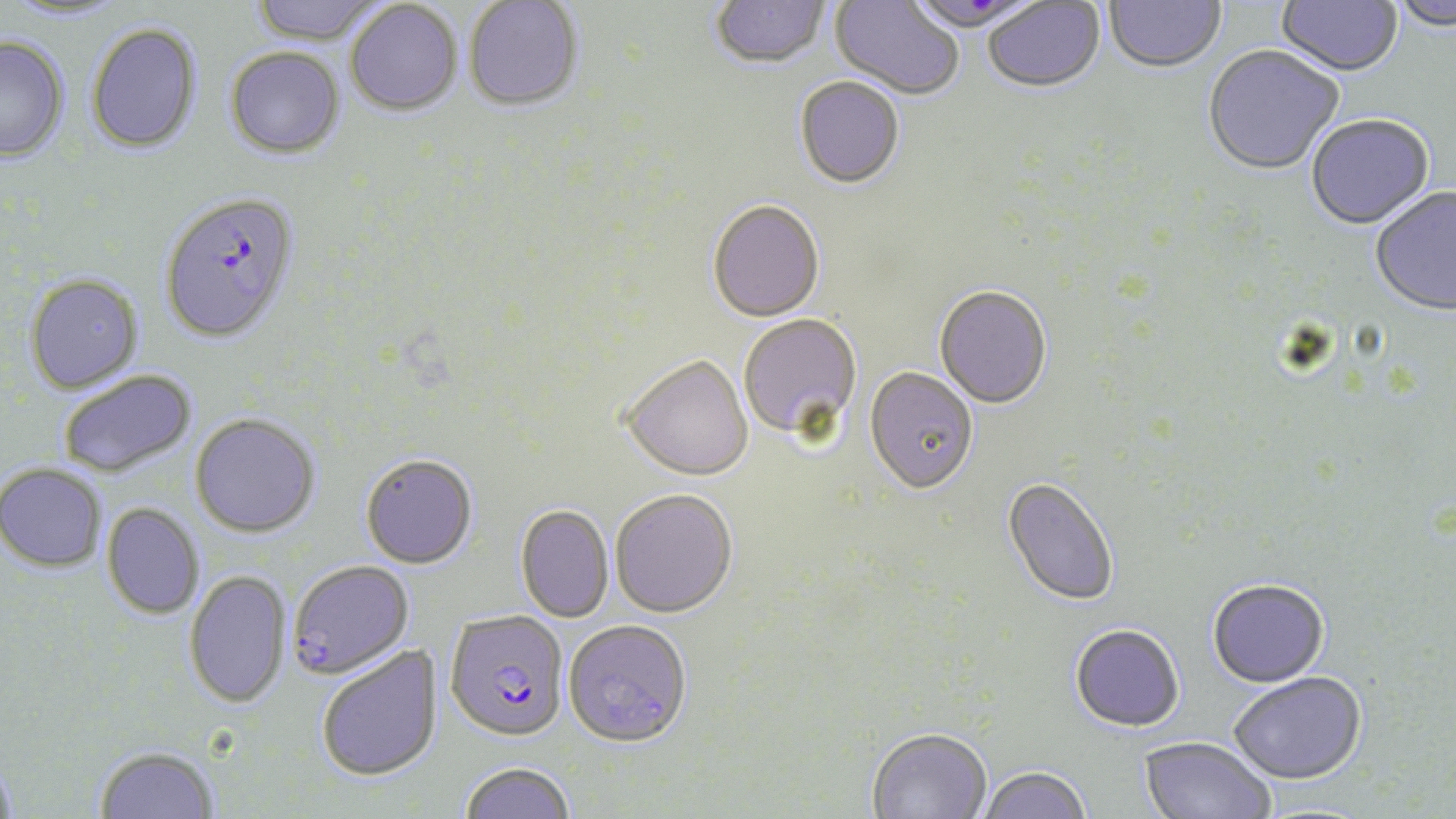 Approximate bounding boxes as [x1, y1, x2, y2] in pixels. Plasmodium falciparum-infected red blood cell locations: [159, 192, 300, 343], [288, 560, 414, 679], [444, 611, 569, 744]. Uninfected red blood cell locations: [3, 0, 130, 23], [249, 0, 389, 46], [1104, 0, 1226, 76], [1276, 0, 1404, 79], [464, 1, 584, 114], [711, 1, 830, 72], [829, 1, 964, 102], [983, 1, 1106, 96], [1390, 1, 1456, 34], [345, 2, 463, 118], [85, 22, 202, 153], [0, 36, 69, 161], [224, 47, 346, 160], [1203, 47, 1344, 177], [794, 78, 904, 191], [1306, 117, 1434, 232], [1370, 188, 1456, 319], [707, 202, 825, 324], [24, 273, 143, 393], [934, 288, 1052, 411], [738, 315, 863, 445], [621, 357, 753, 483], [864, 369, 978, 497], [58, 370, 197, 478], [190, 413, 321, 537], [361, 455, 477, 570], [0, 462, 107, 572], [1001, 478, 1118, 609], [610, 491, 738, 620], [103, 503, 204, 619], [515, 505, 614, 623], [184, 569, 292, 708], [1207, 580, 1330, 690], [564, 621, 693, 750], [1070, 626, 1185, 734], [315, 644, 443, 783], [1229, 674, 1367, 787], [867, 730, 992, 819], [1138, 738, 1274, 819], [94, 745, 219, 819], [0, 755, 16, 819], [459, 762, 576, 819], [978, 769, 1091, 819]. Slide-level diagnosis: Plasmodium falciparum. One field of a larger specimen. Thin blood film. Image is 1456×819 pixels. May-Grünwald-Giemsa stain. 1000x magnification. Light microscopy.